Find the cells and give the type of each one.
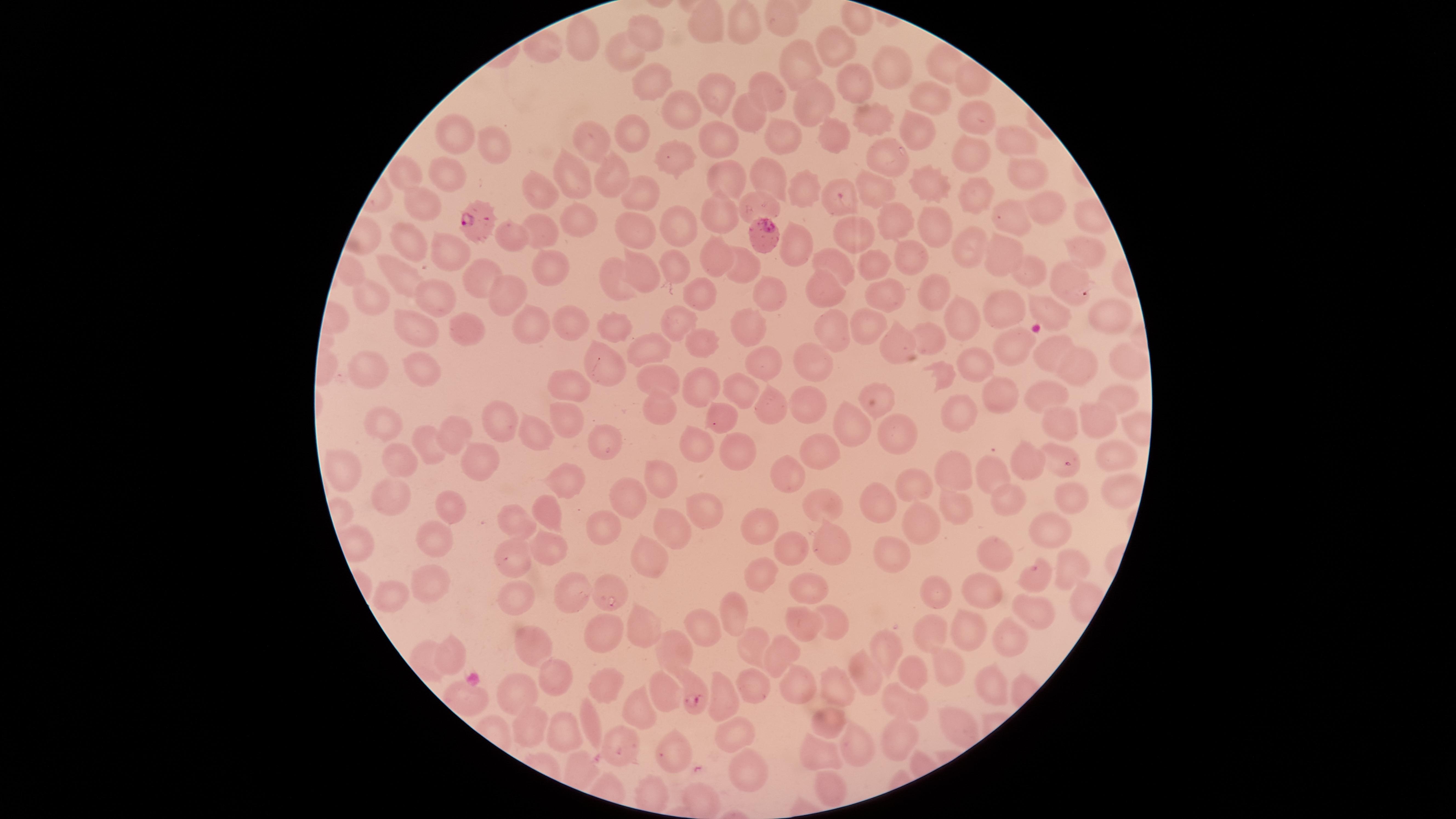

Approximate marker points, in pixels from the top-left corner.
Parasitized red blood cells: (x=841, y=196), (x=482, y=220), (x=765, y=233), (x=694, y=696).
Uninfected red blood cells: (x=708, y=26), (x=749, y=27), (x=649, y=33), (x=584, y=39), (x=838, y=53), (x=624, y=59), (x=805, y=61), (x=889, y=73), (x=860, y=85), (x=654, y=86), (x=717, y=90), (x=770, y=90), (x=814, y=101), (x=929, y=101), (x=683, y=107), (x=752, y=114), (x=971, y=116), (x=867, y=117), (x=1225, y=119), (x=918, y=128), (x=635, y=129), (x=457, y=135), (x=837, y=135), (x=717, y=136), (x=784, y=136), (x=1019, y=139), (x=597, y=141), (x=494, y=148), (x=881, y=157), (x=675, y=158), (x=975, y=161), (x=1024, y=166), (x=407, y=169), (x=453, y=173), (x=769, y=173), (x=576, y=178), (x=610, y=179), (x=722, y=179), (x=875, y=183), (x=934, y=185), (x=803, y=189), (x=539, y=192), (x=638, y=195), (x=975, y=197), (x=422, y=205), (x=767, y=205), (x=1041, y=205), (x=717, y=211), (x=892, y=218), (x=578, y=221), (x=1007, y=222), (x=679, y=226), (x=935, y=228), (x=539, y=230), (x=863, y=232), (x=634, y=233), (x=511, y=234), (x=412, y=235), (x=963, y=242), (x=794, y=247), (x=449, y=250), (x=909, y=252), (x=1087, y=252), (x=713, y=255), (x=1002, y=256), (x=837, y=260), (x=546, y=264), (x=878, y=264), (x=675, y=266), (x=642, y=268), (x=742, y=269), (x=476, y=274), (x=1077, y=275), (x=401, y=276), (x=1033, y=277), (x=613, y=282), (x=438, y=290), (x=767, y=290), (x=824, y=290), (x=510, y=292), (x=934, y=293), (x=698, y=296), (x=882, y=297), (x=371, y=304), (x=1054, y=310), (x=1005, y=311), (x=1104, y=313), (x=683, y=316), (x=975, y=319), (x=468, y=320), (x=531, y=322), (x=576, y=327), (x=421, y=331), (x=613, y=331), (x=748, y=331), (x=865, y=331), (x=836, y=332), (x=928, y=336), (x=701, y=339), (x=899, y=340), (x=650, y=346), (x=1013, y=347), (x=761, y=356), (x=1049, y=357), (x=1124, y=360), (x=600, y=364), (x=813, y=365), (x=979, y=366), (x=373, y=367), (x=1082, y=372), (x=426, y=375), (x=942, y=378), (x=567, y=381), (x=705, y=382), (x=661, y=383), (x=742, y=385), (x=991, y=393), (x=1045, y=397), (x=1114, y=400), (x=806, y=405), (x=769, y=406), (x=663, y=410), (x=957, y=410), (x=717, y=415), (x=574, y=418), (x=497, y=422), (x=1097, y=422), (x=1065, y=423), (x=385, y=426), (x=538, y=428), (x=845, y=428), (x=900, y=433), (x=454, y=434), (x=605, y=438), (x=700, y=443), (x=426, y=445), (x=738, y=449), (x=397, y=451), (x=1057, y=457), (x=1108, y=458), (x=1029, y=459), (x=816, y=461), (x=345, y=467), (x=475, y=468), (x=953, y=471), (x=566, y=476), (x=987, y=476), (x=666, y=479), (x=912, y=479), (x=787, y=483), (x=1120, y=491), (x=384, y=496), (x=629, y=498), (x=819, y=498), (x=1074, y=498), (x=1011, y=502), (x=704, y=503), (x=881, y=505), (x=954, y=507), (x=544, y=511), (x=444, y=512), (x=510, y=514), (x=919, y=525), (x=763, y=527), (x=1050, y=528), (x=601, y=530), (x=668, y=530), (x=825, y=542), (x=431, y=544), (x=794, y=547), (x=544, y=550), (x=892, y=552), (x=997, y=555), (x=645, y=560), (x=507, y=568), (x=1071, y=568), (x=763, y=572), (x=1035, y=577), (x=810, y=585), (x=430, y=588), (x=572, y=588), (x=981, y=588), (x=521, y=594), (x=393, y=597), (x=935, y=598), (x=1029, y=609), (x=738, y=611), (x=823, y=623), (x=800, y=626), (x=639, y=628), (x=696, y=631), (x=929, y=633), (x=963, y=634), (x=595, y=638), (x=1000, y=639), (x=530, y=640), (x=885, y=640), (x=747, y=642), (x=675, y=649), (x=783, y=649), (x=447, y=653), (x=947, y=667), (x=869, y=672), (x=904, y=672), (x=551, y=679), (x=799, y=684), (x=598, y=686), (x=836, y=687), (x=992, y=687), (x=666, y=688), (x=748, y=691), (x=516, y=692), (x=904, y=697), (x=466, y=699), (x=723, y=699), (x=642, y=701), (x=592, y=715), (x=955, y=721), (x=825, y=724), (x=529, y=726), (x=563, y=733), (x=735, y=733), (x=899, y=738), (x=858, y=743), (x=616, y=744), (x=863, y=747), (x=671, y=755), (x=819, y=755), (x=747, y=771), (x=830, y=786), (x=701, y=795).
No white blood cells identified.

image size = 1456×819 pixels
field of view = single
capture = smartphone photograph through the microscope eyepiece
species = Plasmodium falciparum
visible region = circular
stain = Giemsa
preparation = thin smear of blood